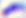 Micrograph. Toxoplasma gondii is shown. 400x magnification.